Outline platelets.
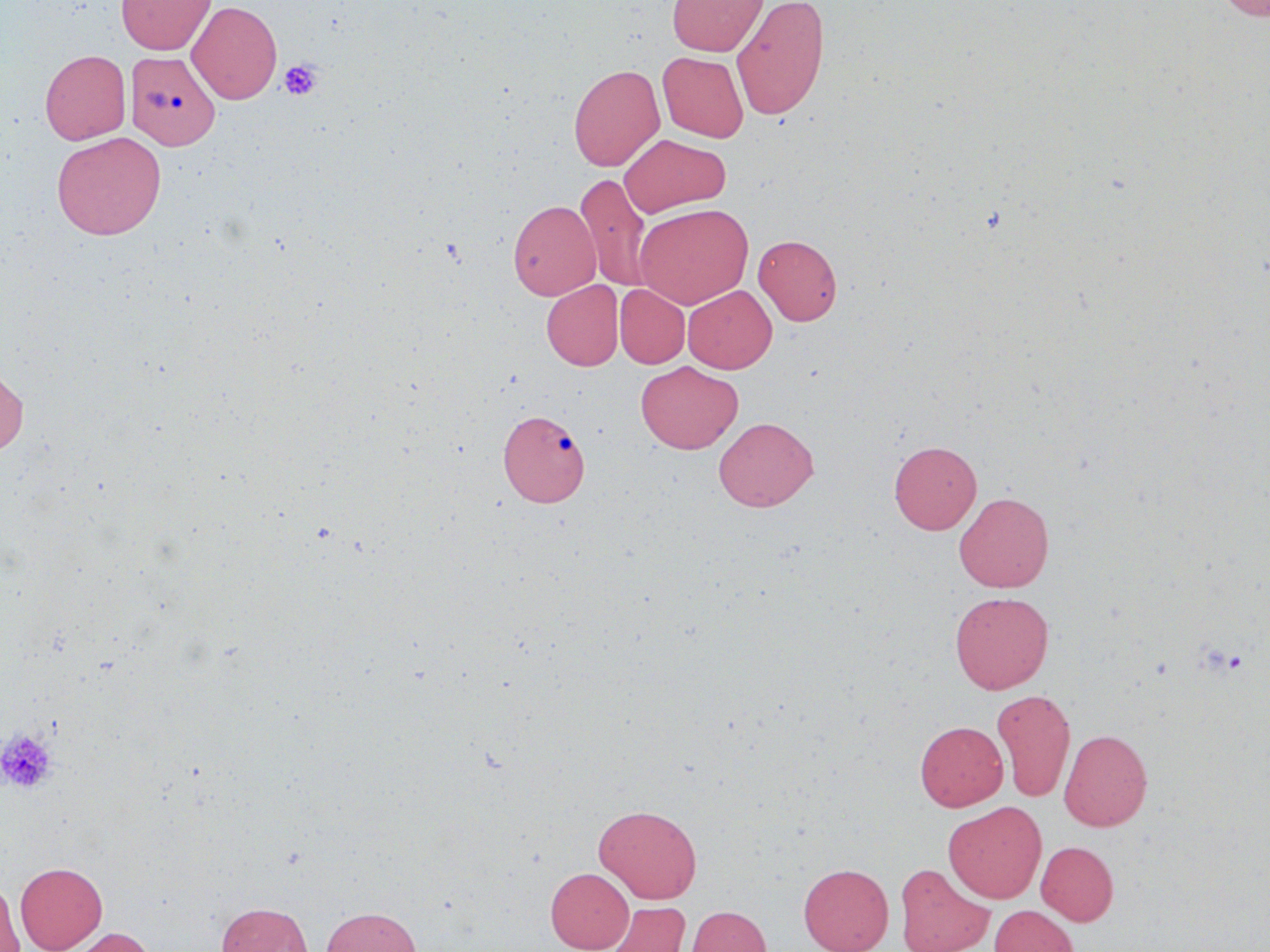

Approximate bounding boxes as (x1,y1)-(x2,y2) corner pairs in pixels.
Platelets: (279,59)-(322,100), (0,729)-(58,794).

slide-level diagnosis = negative for blood parasites
field of view = one of a larger specimen
preparation = thin blood film
modality = light microscopy
stain = May-Grünwald-Giemsa
magnification = 1000x
image size = 1270×952 pixels
uninfected red blood cell locations = approximate bounding boxes as (x1,y1)-(x2,y2) corner pairs in pixels: (116,0)-(216,55), (667,0)-(768,56), (1215,0)-(1270,19), (187,1)-(282,104), (732,1)-(830,120), (40,49)-(130,144), (125,51)-(220,149), (657,51)-(749,142), (568,63)-(665,171), (51,131)-(167,240), (619,133)-(731,217), (576,173)-(653,293), (507,199)-(601,300), (634,203)-(753,308), (753,234)-(843,325), (542,280)-(623,370), (615,284)-(690,368), (683,285)-(777,373), (635,361)-(743,454), (0,364)-(29,457), (498,409)-(589,507), (713,416)-(819,511), (889,440)-(982,534), (954,491)-(1054,592), (949,591)-(1054,694), (992,688)-(1076,802), (915,720)-(1008,811), (1059,728)-(1153,831), (943,801)-(1046,903), (593,803)-(702,904), (1036,841)-(1119,925), (15,861)-(107,952), (894,862)-(994,952), (798,863)-(894,952), (546,867)-(634,952), (0,878)-(24,952), (602,901)-(690,952), (216,902)-(312,952), (686,905)-(771,952), (988,905)-(1079,952), (321,906)-(422,952), (64,926)-(157,952)